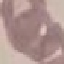
{
  "result": "no malaria parasites seen",
  "preparation": "thin blood film",
  "capture": "smartphone camera at the microscope eyepiece",
  "stain": "Giemsa",
  "image_type": "automatically extracted cell patch, resized to 64 × 64 pixels"
}